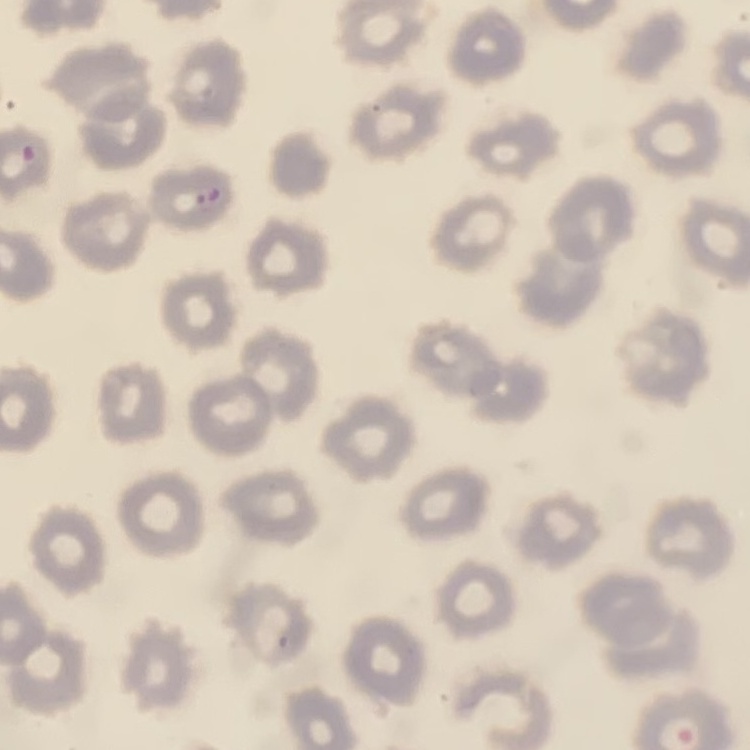
Summary:
  - Red blood cell morphology: no rouleaux formation
  - Preparation: thin peripheral smear
  - Stain: Field's or Giemsa
  - Image type: square crop of a larger photomicrograph